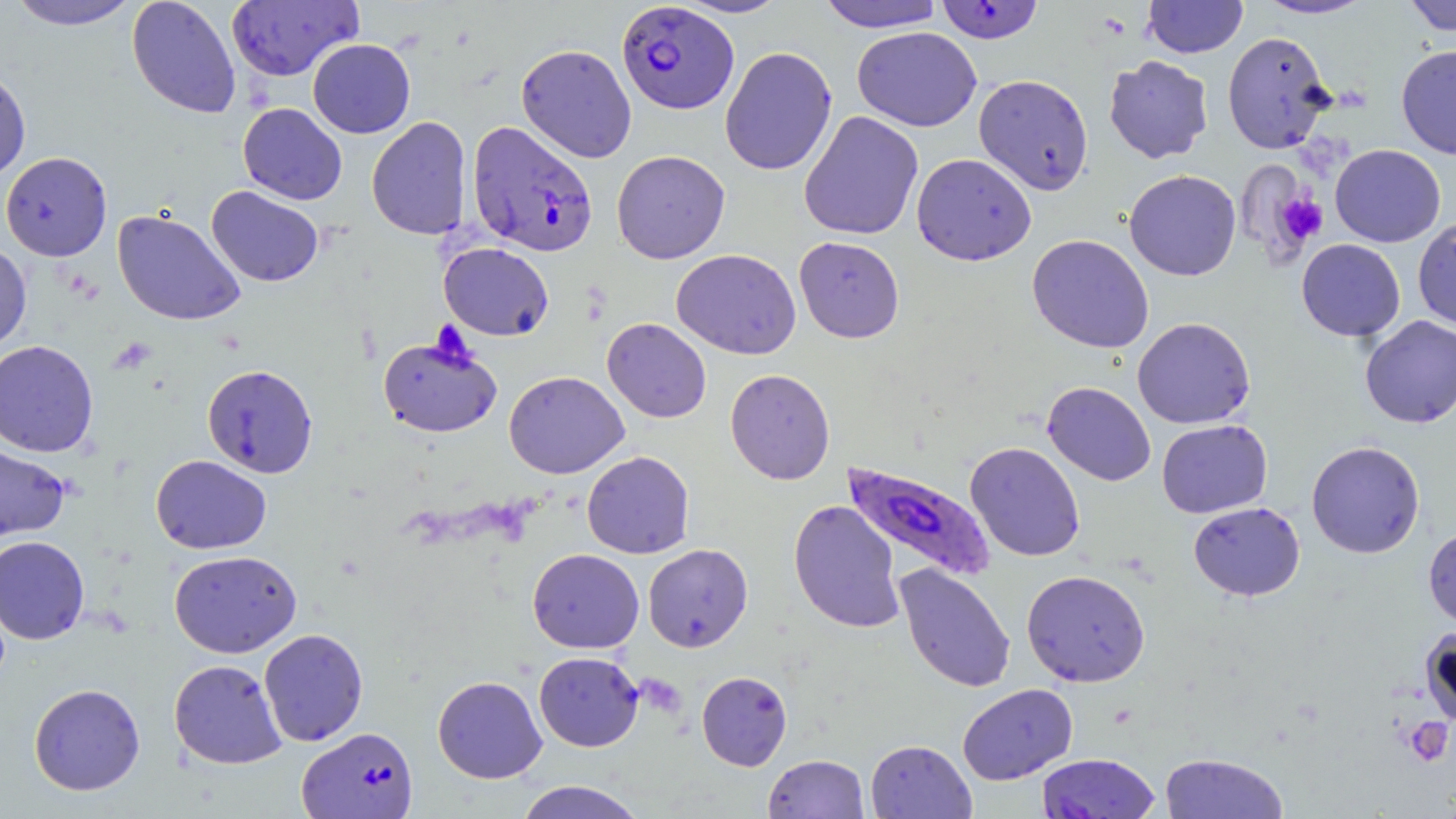
Summary:
  - Coordinate format: approximate bounding boxes as named x1/y1/x2/y2 corners in pixels
  - Uninfected red blood cell locations: (x1=6, y1=0, x2=142, y2=30), (x1=127, y1=0, x2=241, y2=119), (x1=674, y1=0, x2=791, y2=18), (x1=816, y1=0, x2=944, y2=32), (x1=1143, y1=0, x2=1248, y2=58), (x1=1256, y1=0, x2=1374, y2=19), (x1=1402, y1=0, x2=1456, y2=36), (x1=226, y1=1, x2=362, y2=82), (x1=852, y1=26, x2=982, y2=131), (x1=1222, y1=31, x2=1334, y2=154), (x1=308, y1=38, x2=415, y2=138), (x1=516, y1=44, x2=637, y2=163), (x1=1396, y1=44, x2=1456, y2=159), (x1=719, y1=46, x2=837, y2=176), (x1=1103, y1=55, x2=1214, y2=164), (x1=0, y1=68, x2=31, y2=182), (x1=973, y1=73, x2=1094, y2=195), (x1=238, y1=103, x2=347, y2=205), (x1=799, y1=111, x2=924, y2=241), (x1=366, y1=116, x2=472, y2=240), (x1=1330, y1=144, x2=1446, y2=247), (x1=611, y1=150, x2=730, y2=264), (x1=1, y1=151, x2=112, y2=261), (x1=911, y1=153, x2=1037, y2=265), (x1=1124, y1=169, x2=1241, y2=281), (x1=206, y1=185, x2=324, y2=287), (x1=112, y1=209, x2=245, y2=325), (x1=1413, y1=217, x2=1456, y2=331), (x1=1026, y1=234, x2=1154, y2=353), (x1=794, y1=236, x2=905, y2=343), (x1=1296, y1=239, x2=1405, y2=341), (x1=0, y1=240, x2=32, y2=355), (x1=438, y1=242, x2=554, y2=340), (x1=671, y1=249, x2=801, y2=359), (x1=1359, y1=316, x2=1456, y2=429), (x1=602, y1=317, x2=712, y2=423), (x1=1132, y1=317, x2=1255, y2=429), (x1=378, y1=334, x2=503, y2=437), (x1=0, y1=339, x2=98, y2=457), (x1=202, y1=364, x2=318, y2=478), (x1=725, y1=368, x2=836, y2=485), (x1=504, y1=371, x2=629, y2=479), (x1=1042, y1=381, x2=1156, y2=486), (x1=1157, y1=419, x2=1272, y2=518), (x1=1306, y1=440, x2=1425, y2=559), (x1=965, y1=441, x2=1086, y2=561), (x1=0, y1=443, x2=70, y2=542), (x1=582, y1=450, x2=695, y2=559), (x1=151, y1=454, x2=271, y2=554), (x1=788, y1=499, x2=905, y2=634), (x1=1188, y1=501, x2=1305, y2=601), (x1=1423, y1=525, x2=1456, y2=631), (x1=0, y1=535, x2=90, y2=643), (x1=642, y1=543, x2=753, y2=652), (x1=527, y1=548, x2=644, y2=653), (x1=169, y1=550, x2=301, y2=658), (x1=894, y1=563, x2=1016, y2=693), (x1=1021, y1=569, x2=1150, y2=687), (x1=1419, y1=625, x2=1456, y2=726), (x1=258, y1=628, x2=368, y2=746), (x1=534, y1=651, x2=643, y2=752), (x1=168, y1=659, x2=287, y2=769), (x1=697, y1=670, x2=792, y2=771), (x1=432, y1=675, x2=547, y2=783), (x1=29, y1=683, x2=145, y2=796), (x1=957, y1=683, x2=1078, y2=784), (x1=865, y1=739, x2=976, y2=818), (x1=1159, y1=752, x2=1289, y2=818), (x1=1036, y1=753, x2=1160, y2=818), (x1=763, y1=754, x2=870, y2=818), (x1=513, y1=780, x2=648, y2=819)
  - Platelet locations: (x1=1277, y1=192, x2=1328, y2=245), (x1=1404, y1=717, x2=1453, y2=767)
  - Plasmodium falciparum-infected red blood cell locations: (x1=935, y1=1, x2=1044, y2=44), (x1=616, y1=2, x2=739, y2=115), (x1=467, y1=120, x2=599, y2=258), (x1=841, y1=460, x2=996, y2=582), (x1=297, y1=726, x2=418, y2=818)
  - Slide-level diagnosis: Plasmodium falciparum
  - Stain: May-Grünwald-Giemsa
  - Modality: optical microscopy
  - Image size: 1456×819 pixels
  - Preparation: thin blood film
  - Field of view: single
  - Magnification: 1000x